Locate every Plasmodium parasite.
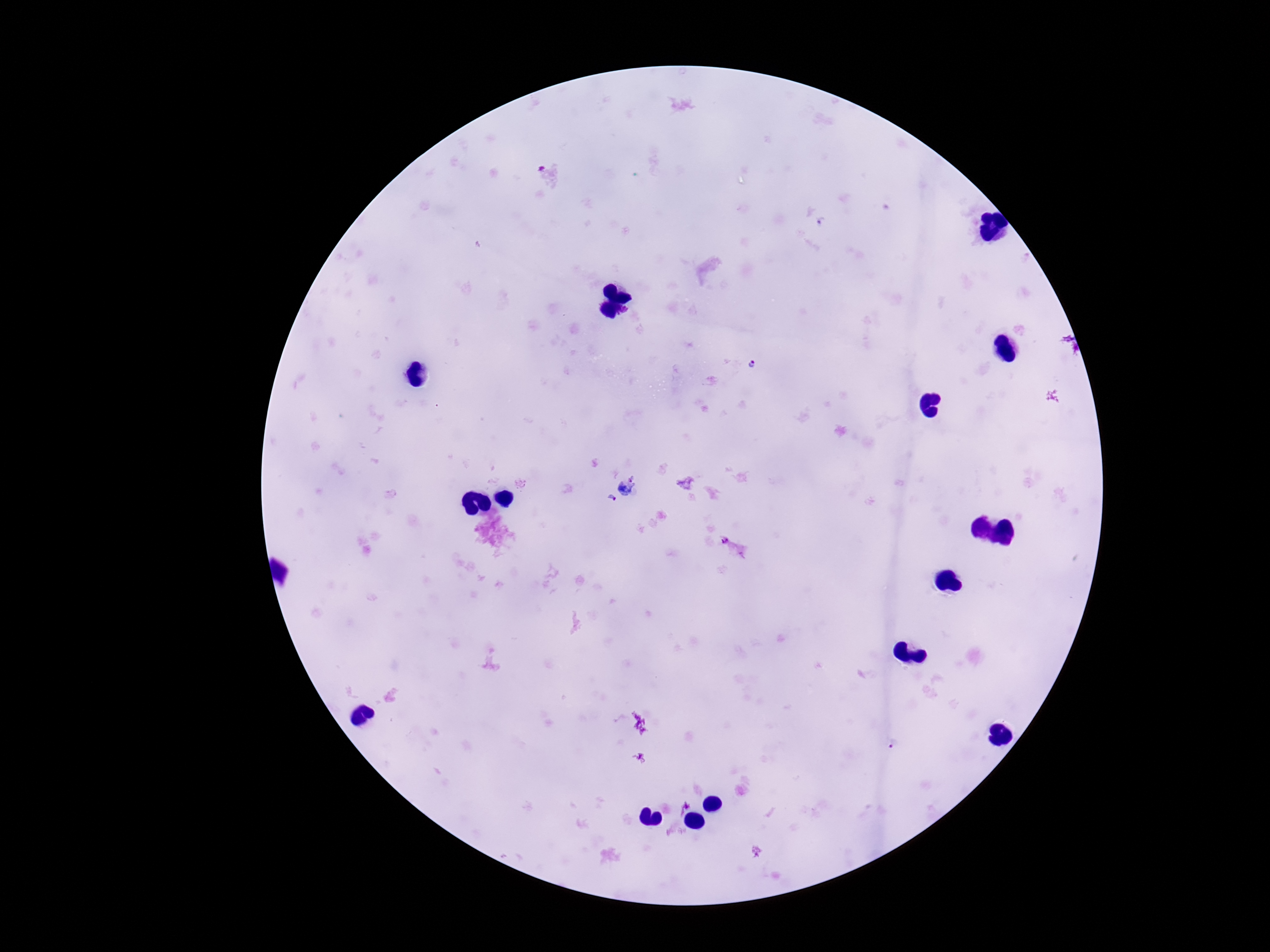

Approximate object centers, in pixels from the top-left corner.
Plasmodium parasites: (x=753, y=364), (x=626, y=488), (x=613, y=498), (x=725, y=539).

Summary:
  - Preparation: thick peripheral-blood smear
  - Capture: smartphone camera through the microscope eyepiece
  - Magnification: 100x
  - Stain: Giemsa
  - Patient malaria status: infected
  - Image size: 1270×952 pixels
  - Field of view: single